Outline each Plasmodium vivax-infected red blood cell.
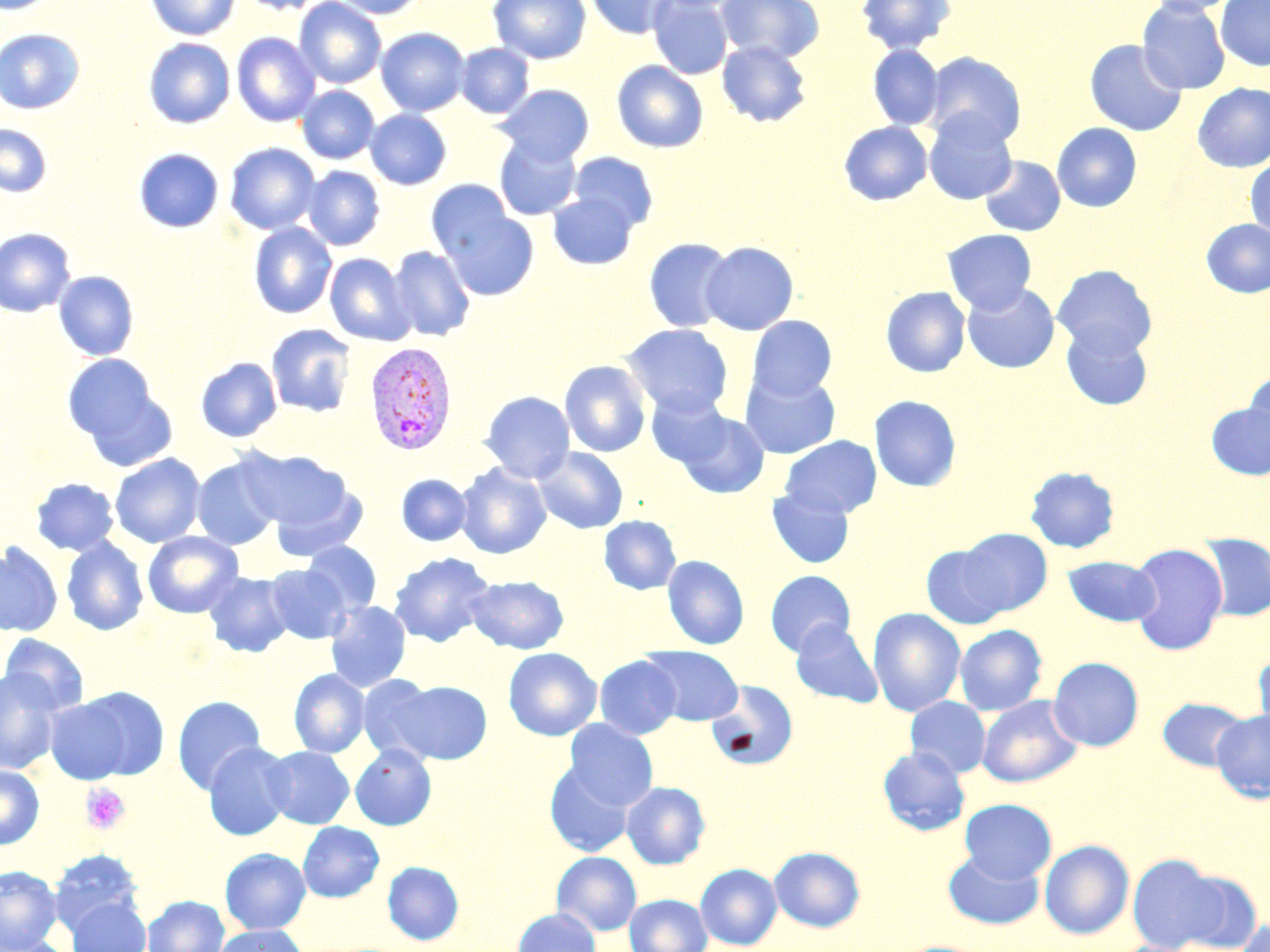

Approximate bounding boxes as (x1, y1, x2, y2) in pixels.
Plasmodium vivax-infected red blood cells: (364, 341, 457, 455).

Summary:
  - Platelet locations: (80, 782, 131, 835)
  - Uninfected red blood cell locations: (0, 0, 57, 14), (145, 0, 240, 40), (237, 0, 329, 15), (294, 0, 386, 89), (332, 0, 427, 19), (488, 0, 592, 65), (585, 0, 676, 39), (648, 0, 733, 79), (715, 0, 825, 63), (856, 0, 956, 55), (1137, 0, 1231, 95), (1146, 0, 1240, 15), (1216, 0, 1270, 71), (376, 27, 470, 117), (0, 28, 86, 114), (232, 32, 321, 127), (143, 38, 235, 128), (1084, 39, 1187, 136), (717, 40, 812, 127), (456, 43, 534, 118), (867, 44, 944, 130), (924, 51, 1027, 148), (612, 60, 708, 153), (1193, 83, 1270, 172), (496, 84, 594, 165), (297, 85, 379, 164), (365, 109, 452, 190), (923, 111, 1018, 205), (838, 121, 933, 206), (1052, 122, 1142, 212), (0, 124, 52, 198), (494, 135, 582, 221), (225, 142, 320, 234), (134, 148, 224, 233), (568, 152, 658, 233), (979, 156, 1065, 236), (1245, 157, 1270, 239), (303, 166, 385, 251), (425, 179, 515, 261), (547, 193, 639, 270), (439, 207, 540, 301), (1200, 219, 1270, 298), (248, 222, 337, 319), (0, 228, 76, 317), (942, 229, 1037, 315), (643, 237, 736, 333), (701, 241, 799, 336), (389, 246, 475, 342), (324, 253, 415, 346), (1052, 264, 1156, 358), (53, 271, 139, 360), (962, 282, 1060, 374), (880, 286, 971, 377), (747, 315, 837, 401), (1060, 322, 1153, 410), (266, 323, 356, 417), (622, 323, 734, 418), (61, 353, 169, 458), (196, 357, 282, 442), (559, 360, 651, 457), (740, 370, 840, 459), (1243, 370, 1270, 454), (480, 391, 575, 483), (646, 392, 733, 468), (869, 395, 961, 492), (1206, 403, 1270, 480), (674, 410, 770, 498), (780, 435, 882, 518), (533, 446, 628, 534), (240, 449, 353, 536), (110, 453, 206, 547), (192, 457, 283, 550), (455, 463, 551, 559), (1024, 466, 1120, 554), (397, 474, 472, 546), (30, 478, 119, 556), (266, 478, 369, 564), (766, 486, 855, 568), (599, 515, 681, 595), (957, 528, 1053, 616), (142, 531, 243, 619), (1198, 535, 1270, 621), (61, 536, 148, 636), (302, 541, 381, 615), (0, 543, 63, 637), (920, 543, 1013, 630), (1128, 544, 1229, 655), (389, 551, 495, 647), (662, 555, 749, 650), (1063, 556, 1161, 627), (266, 564, 352, 644), (204, 570, 294, 657), (765, 570, 856, 657), (466, 575, 568, 653), (325, 600, 411, 692), (867, 608, 966, 717), (790, 622, 883, 708), (954, 624, 1048, 716), (1, 633, 90, 715), (641, 646, 743, 725), (503, 647, 602, 741), (1253, 650, 1270, 738), (595, 656, 683, 739), (1048, 657, 1144, 751), (0, 668, 64, 775), (289, 668, 370, 758), (357, 674, 441, 763), (394, 680, 492, 764), (706, 680, 798, 771), (44, 695, 140, 784), (173, 695, 266, 794), (977, 695, 1083, 788), (905, 696, 991, 778), (1157, 697, 1249, 772), (1211, 709, 1270, 803), (564, 719, 658, 810), (203, 741, 295, 840), (350, 744, 437, 831), (877, 745, 971, 836), (264, 746, 354, 828), (545, 760, 636, 856), (0, 765, 44, 849), (621, 781, 710, 869), (960, 798, 1057, 883), (298, 821, 384, 902), (1039, 840, 1134, 940), (769, 847, 866, 932), (220, 848, 310, 934), (50, 849, 144, 932), (943, 850, 1044, 930), (551, 851, 642, 936), (1127, 853, 1230, 952), (382, 861, 464, 946), (695, 863, 782, 950), (0, 866, 62, 952), (624, 893, 712, 952), (144, 895, 229, 952), (66, 897, 150, 952), (511, 907, 601, 952), (1236, 918, 1270, 952), (212, 925, 307, 952), (0, 936, 75, 952)
  - Slide-level diagnosis: Plasmodium vivax
  - Image size: 1270×952 pixels
  - Field of view: single
  - Modality: optical microscopy
  - Preparation: thin blood film
  - Stain: May-Grünwald-Giemsa
  - Magnification: 1000x